Identify the cell.
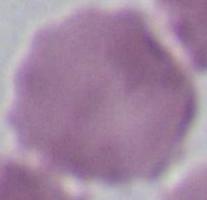
An erythrocyte.

modality: photomicrograph
magnification: 1000x